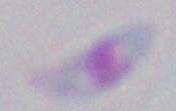
Summary:
  - Magnification: 1000x
  - Modality: micrograph
  - Identification: Toxoplasma gondii